Comment on the morphology of the erythrocytes.
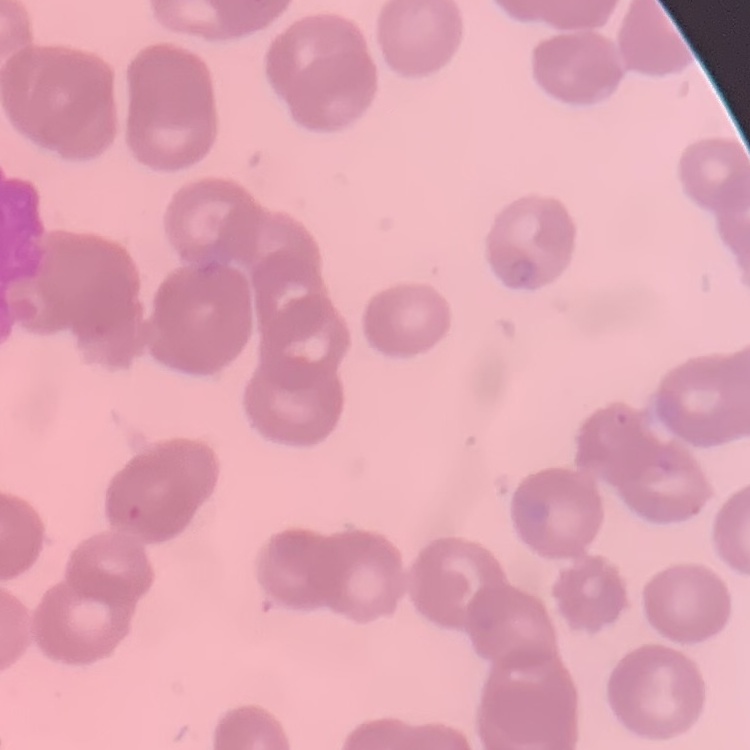
They show rouleaux formation.

stain = Field's or Giemsa
image type = one tile cut from a larger photomicrograph
preparation = thin blood smear